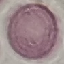
Summary:
  - Malaria status: uninfected
  - Stain: Giemsa
  - Preparation: thin blood film
  - Image type: cell patch, automatically extracted from a larger field of view and resized to 64 × 64 pixels
  - Capture: smartphone camera at the microscope eyepiece